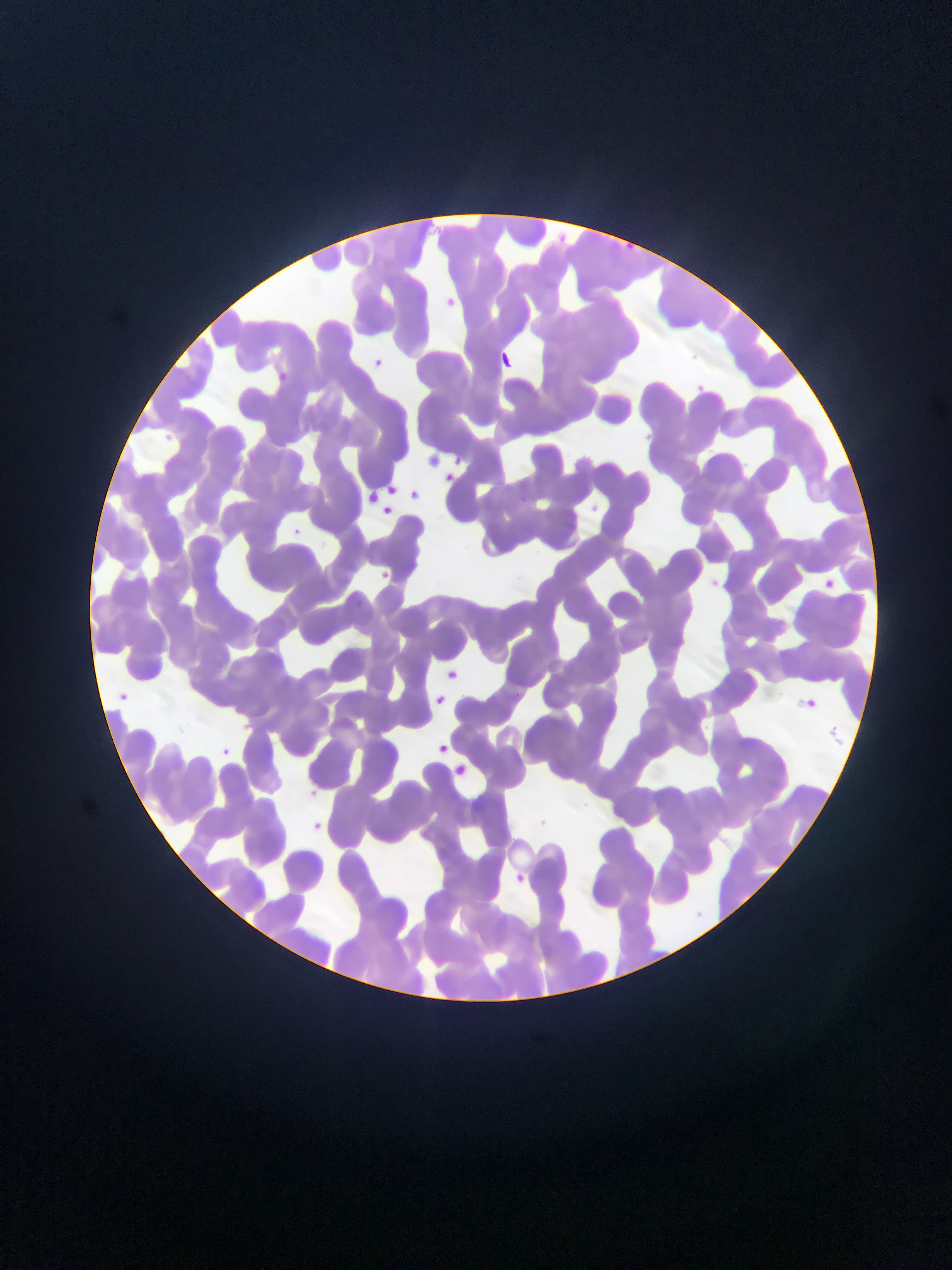

Approximate bounding boxes as {left, top, right, bottom} in pixels. Plasmodium parasite locations: {626, 235, 644, 256}, {442, 294, 463, 316}, {503, 345, 514, 372}, {372, 358, 389, 378}, {277, 371, 290, 382}, {696, 380, 715, 399}, {162, 429, 177, 440}, {516, 490, 530, 504}, {292, 524, 304, 540}, {375, 567, 392, 579}, {118, 691, 134, 703}, {829, 720, 842, 748}, {220, 741, 238, 764}, {314, 787, 325, 805}, {306, 810, 324, 827}, {545, 811, 553, 822}. Collected in Ghana. Mobile-phone photograph taken through the microscope. Thin blood smear. Single field of view. Image is 952×1270 pixels.